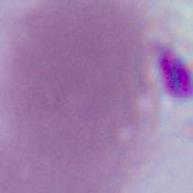
Summary:
  - Modality: photomicrograph
  - Magnification: 1000x
  - Identification: erythrocyte